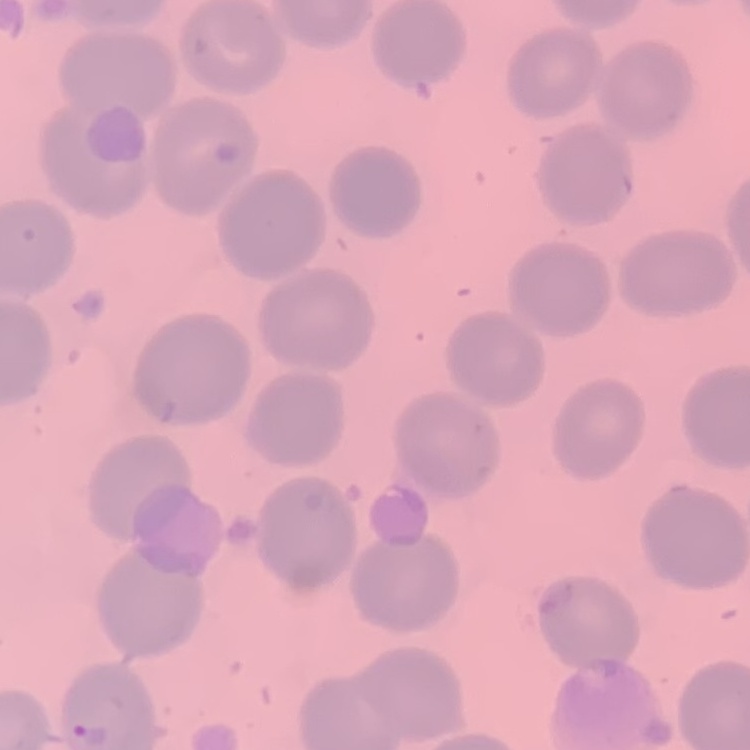

erythrocyte morphology = no rouleaux formation
stain = Field's or Giemsa
image type = square crop of a larger photomicrograph
preparation = thin peripheral smear